Assess the morphology of the erythrocytes.
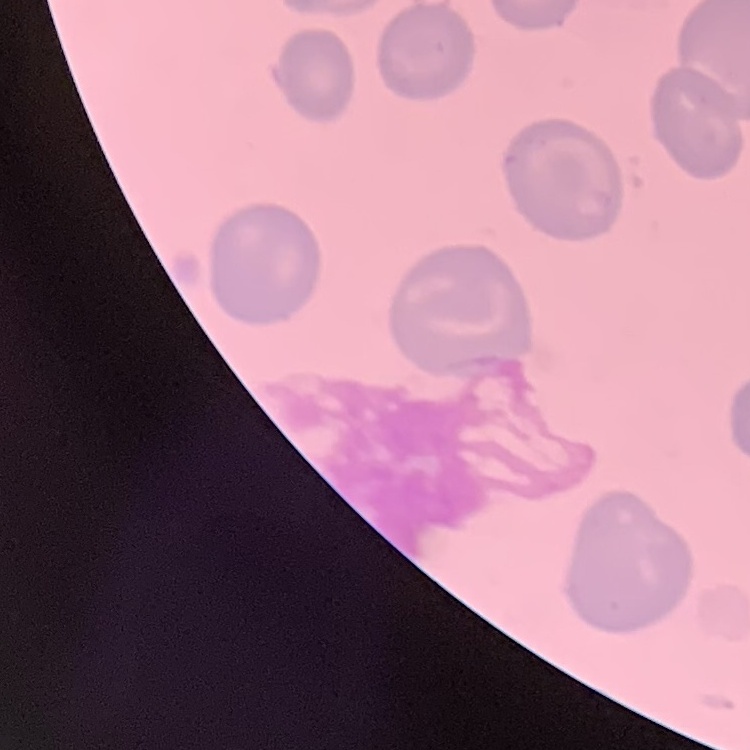
They show no rouleaux formation.

preparation = thin blood smear
image type = square crop of a larger photomicrograph
stain = Field's or Giemsa